Comment on the morphology of the red blood cells.
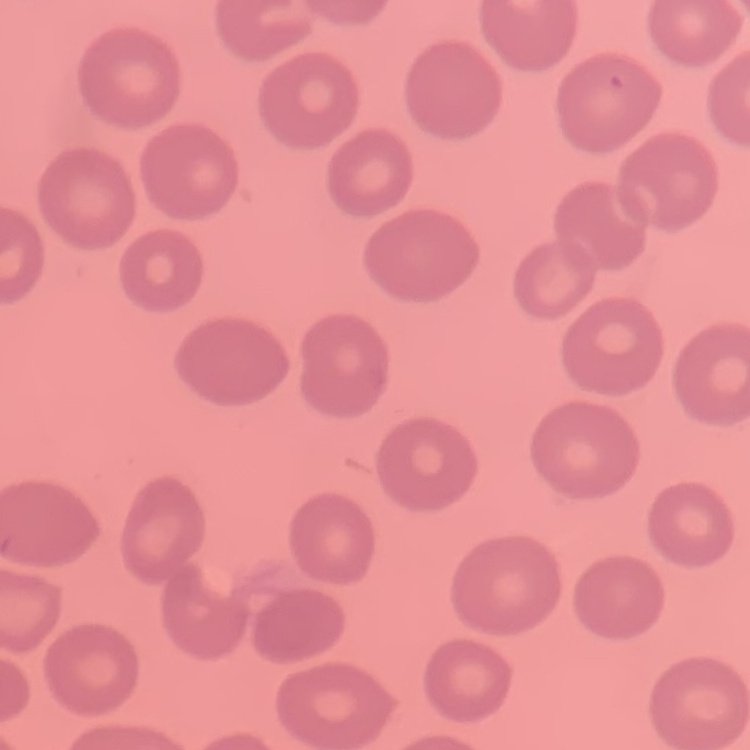

They show no rouleaux formation.

image_type: square crop of a larger photomicrograph
stain: Field's or Giemsa
preparation: thin blood smear